Identify the parasite.
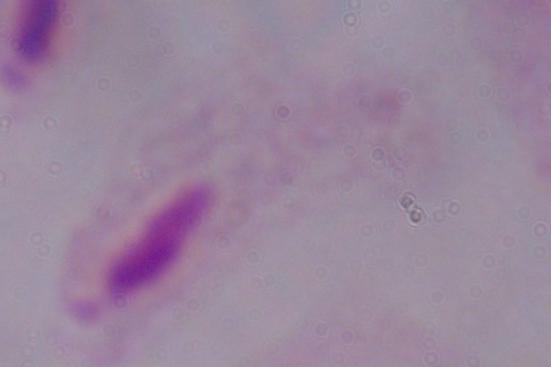
A trichomonad.

Summary:
  - Magnification: 1000x
  - Modality: photomicrograph